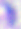
Summary:
  - Modality: photomicrograph
  - Magnification: 400x
  - Identification: Toxoplasma gondii